Locate every Plasmodium falciparum-infected red blood cell.
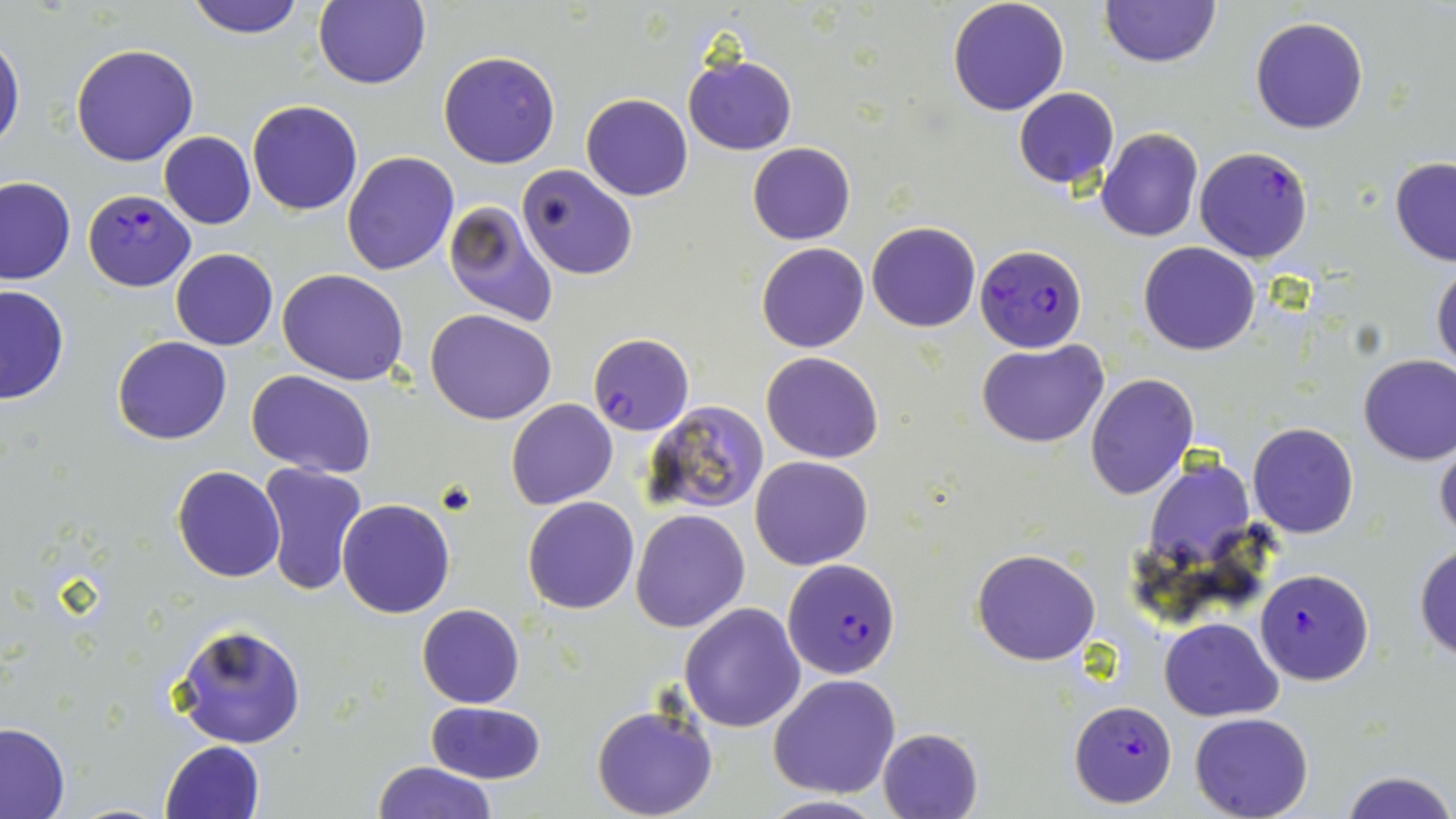

Approximate bounding boxes as named x1/y1/x2/y2 corners in pixels.
Plasmodium falciparum-infected red blood cells: (x1=1194, y1=144, x2=1315, y2=264), (x1=83, y1=189, x2=195, y2=292), (x1=975, y1=243, x2=1087, y2=351), (x1=587, y1=333, x2=693, y2=437), (x1=783, y1=558, x2=901, y2=680), (x1=1254, y1=568, x2=1374, y2=686), (x1=1069, y1=702, x2=1177, y2=810).

Uninfected red blood cell locations: (x1=185, y1=0, x2=309, y2=38), (x1=312, y1=0, x2=430, y2=90), (x1=947, y1=0, x2=1070, y2=116), (x1=1101, y1=0, x2=1219, y2=68), (x1=1249, y1=17, x2=1368, y2=135), (x1=0, y1=36, x2=25, y2=156), (x1=71, y1=44, x2=200, y2=165), (x1=438, y1=50, x2=561, y2=169), (x1=682, y1=53, x2=797, y2=155), (x1=1012, y1=87, x2=1120, y2=188), (x1=581, y1=94, x2=693, y2=202), (x1=247, y1=100, x2=362, y2=216), (x1=1097, y1=127, x2=1204, y2=242), (x1=158, y1=131, x2=256, y2=229), (x1=748, y1=142, x2=855, y2=245), (x1=342, y1=150, x2=459, y2=276), (x1=1389, y1=157, x2=1456, y2=266), (x1=518, y1=164, x2=637, y2=280), (x1=0, y1=175, x2=75, y2=285), (x1=443, y1=200, x2=559, y2=327), (x1=867, y1=221, x2=980, y2=332), (x1=1138, y1=240, x2=1261, y2=357), (x1=757, y1=242, x2=869, y2=352), (x1=170, y1=249, x2=277, y2=350), (x1=1431, y1=261, x2=1456, y2=372), (x1=278, y1=269, x2=408, y2=386), (x1=0, y1=284, x2=68, y2=405), (x1=426, y1=309, x2=557, y2=425), (x1=113, y1=336, x2=232, y2=445), (x1=977, y1=340, x2=1110, y2=449), (x1=761, y1=351, x2=884, y2=464), (x1=1357, y1=354, x2=1456, y2=465), (x1=246, y1=370, x2=377, y2=477), (x1=1085, y1=373, x2=1198, y2=500), (x1=505, y1=398, x2=618, y2=510), (x1=643, y1=399, x2=769, y2=518), (x1=1248, y1=422, x2=1359, y2=538), (x1=1435, y1=437, x2=1456, y2=545), (x1=750, y1=455, x2=872, y2=570), (x1=1144, y1=459, x2=1258, y2=580), (x1=258, y1=462, x2=370, y2=598), (x1=172, y1=466, x2=287, y2=583), (x1=521, y1=496, x2=639, y2=614), (x1=337, y1=499, x2=455, y2=619), (x1=629, y1=508, x2=750, y2=632), (x1=1413, y1=543, x2=1456, y2=662), (x1=971, y1=547, x2=1101, y2=665), (x1=678, y1=603, x2=806, y2=733), (x1=416, y1=604, x2=524, y2=708), (x1=1161, y1=617, x2=1281, y2=720), (x1=172, y1=622, x2=307, y2=749), (x1=768, y1=673, x2=900, y2=798), (x1=426, y1=701, x2=547, y2=785), (x1=591, y1=702, x2=719, y2=819), (x1=1190, y1=712, x2=1313, y2=819), (x1=0, y1=723, x2=71, y2=819), (x1=878, y1=728, x2=983, y2=818), (x1=162, y1=740, x2=266, y2=818), (x1=370, y1=760, x2=496, y2=819), (x1=1340, y1=771, x2=1455, y2=819), (x1=755, y1=794, x2=889, y2=818). Slide-level diagnosis: Plasmodium falciparum. Image is 1456×819 pixels. Single field of view. Optical microscopy. Thin blood smear. May-Grünwald-Giemsa stain. 1000x magnification.